Report the malaria status of this cell.
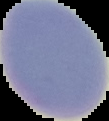

It is uninfected.

image type = cell region segmented out of the field of view; surrounding area masked to black
preparation = thin blood smear
image size = 109×121 pixels